Identify the cell.
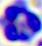
This is a leukocyte.

Summary:
  - Magnification: 400x
  - Modality: photomicrograph